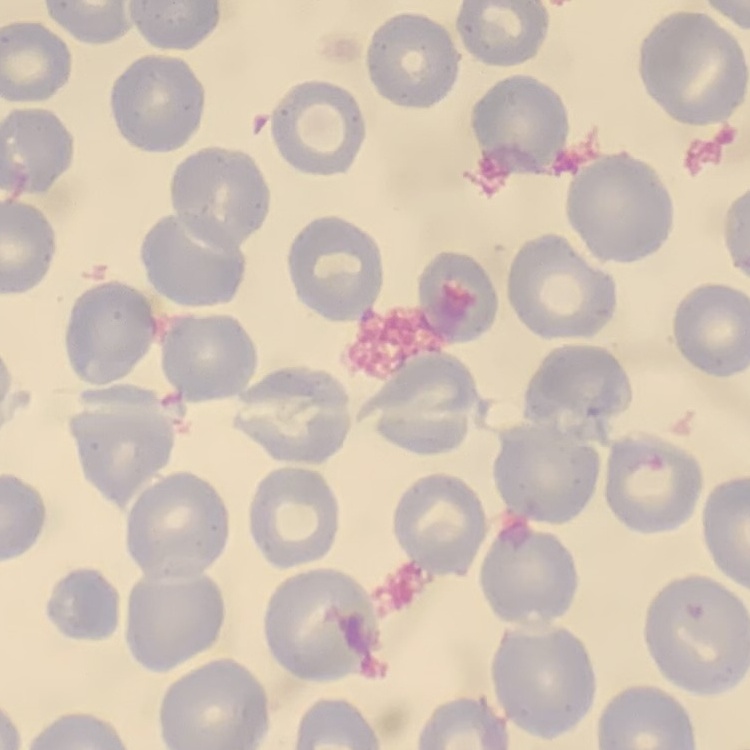

Summary:
  - Red blood cell morphology: no rouleaux formation
  - Stain: Field's or Giemsa
  - Preparation: thin blood smear
  - Image type: square crop of a larger photomicrograph